Identify the parasite.
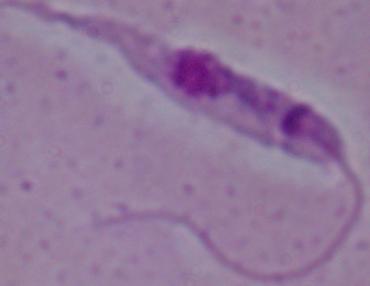

Leishmania.

{
  "magnification": "1000x",
  "modality": "micrograph"
}